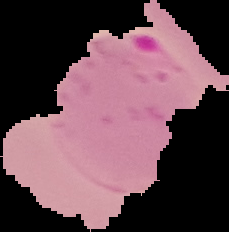
The area outside the segmented cell region is set to black. Image is 229×232 pixels. From a thin blood film. Malaria status: parasitized.